Locate and identify every blood parasite.
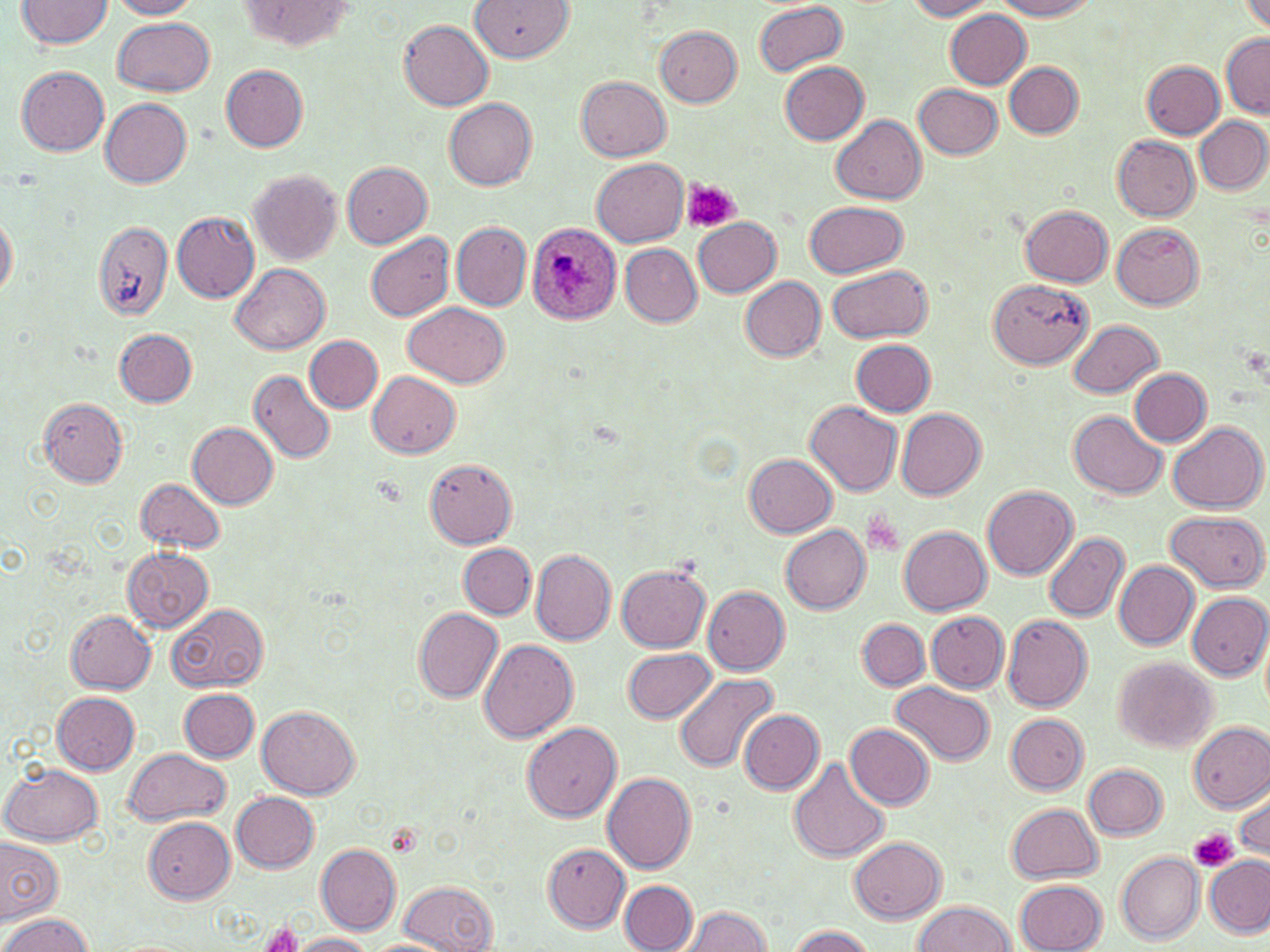

Approximate bounding boxes as (x1,y1)-(x2,y2) corner pairs in pixels.
Plasmodium ovale-infected red blood cells: (526,221)-(623,325).
No Plasmodium falciparum, Plasmodium malariae, Plasmodium vivax, Babesia divergens, or Trypanosoma brucei observed.

slide-level diagnosis = Plasmodium ovale
stain = May-Grünwald-Giemsa
image size = 1270×952 pixels
preparation = thin blood smear
platelet locations = approximate bounding boxes as (x1,y1)-(x2,y2) corner pairs in pixels: (680,178)-(740,235), (1190,829)-(1239,872), (260,923)-(304,952)
field of view = single
uninfected red blood cell locations = approximate bounding boxes as (x1,y1)-(x2,y2) corner pairs in pixels: (18,0)-(114,49), (107,0)-(203,19), (469,0)-(574,62), (903,0)-(998,20), (995,0)-(1097,20), (1236,0)-(1270,34), (237,1)-(359,48), (752,1)-(848,77), (944,8)-(1032,88), (112,16)-(215,96), (398,19)-(494,111), (654,25)-(742,106), (1220,30)-(1269,117), (1140,59)-(1224,139), (778,60)-(869,144), (1005,61)-(1082,138), (219,64)-(309,152), (17,66)-(110,155), (576,75)-(672,162), (913,83)-(1002,159), (101,97)-(193,186), (444,98)-(537,190), (831,115)-(927,204), (1195,117)-(1270,194), (1111,134)-(1200,222), (592,158)-(689,246), (341,160)-(431,248), (247,170)-(341,265), (805,200)-(907,278), (1022,205)-(1113,286), (172,211)-(260,303), (0,212)-(16,301), (693,218)-(782,297), (450,221)-(531,311), (1110,221)-(1203,310), (93,223)-(175,320), (365,232)-(453,321), (620,244)-(702,326), (231,263)-(330,355), (827,264)-(932,345), (739,276)-(826,361), (990,279)-(1092,369), (404,302)-(509,387), (1068,319)-(1163,398), (115,328)-(197,407), (306,335)-(382,413), (851,338)-(936,416), (1129,368)-(1211,445), (249,370)-(336,465), (368,371)-(461,457), (37,399)-(128,487), (806,400)-(902,496), (896,409)-(987,500), (1068,410)-(1167,499), (188,422)-(278,509), (1168,422)-(1267,514), (744,454)-(836,538), (424,460)-(519,549), (135,476)-(225,554), (981,485)-(1078,580), (1164,511)-(1269,591), (780,523)-(870,613), (898,524)-(992,613), (1043,532)-(1130,622), (459,544)-(534,620), (122,547)-(214,632), (531,550)-(617,645), (1113,560)-(1198,650), (617,562)-(713,652), (703,586)-(789,674), (1185,591)-(1269,680), (166,602)-(268,692), (412,607)-(503,702), (66,610)-(156,693), (926,611)-(1011,693), (1001,615)-(1092,711), (857,618)-(930,691), (478,640)-(579,743), (623,648)-(717,725), (1112,657)-(1216,753), (670,671)-(778,773), (890,681)-(995,766), (178,688)-(258,762), (53,693)-(141,775), (257,706)-(360,799), (739,710)-(824,793), (1005,713)-(1088,793), (522,722)-(622,823), (1188,722)-(1270,811), (845,723)-(934,808), (123,748)-(231,827), (788,758)-(891,863), (1,762)-(104,847), (1083,763)-(1168,839), (601,773)-(696,873), (1232,787)-(1269,858), (232,791)-(320,873), (1007,803)-(1104,883), (142,815)-(235,902), (0,836)-(64,924), (849,836)-(946,923), (315,844)-(401,935), (544,844)-(630,932), (1116,852)-(1205,944), (1204,855)-(1269,937), (7,878)-(79,952), (1015,879)-(1106,952), (399,880)-(496,950), (620,881)-(698,952), (912,900)-(1015,952), (679,907)-(773,951), (3,914)-(93,951), (784,926)-(873,952), (292,933)-(377,952), (362,939)-(451,952)
magnification = 1000x
modality = light microscopy